Draw a bounding box around every leukocyte (white blood cell).
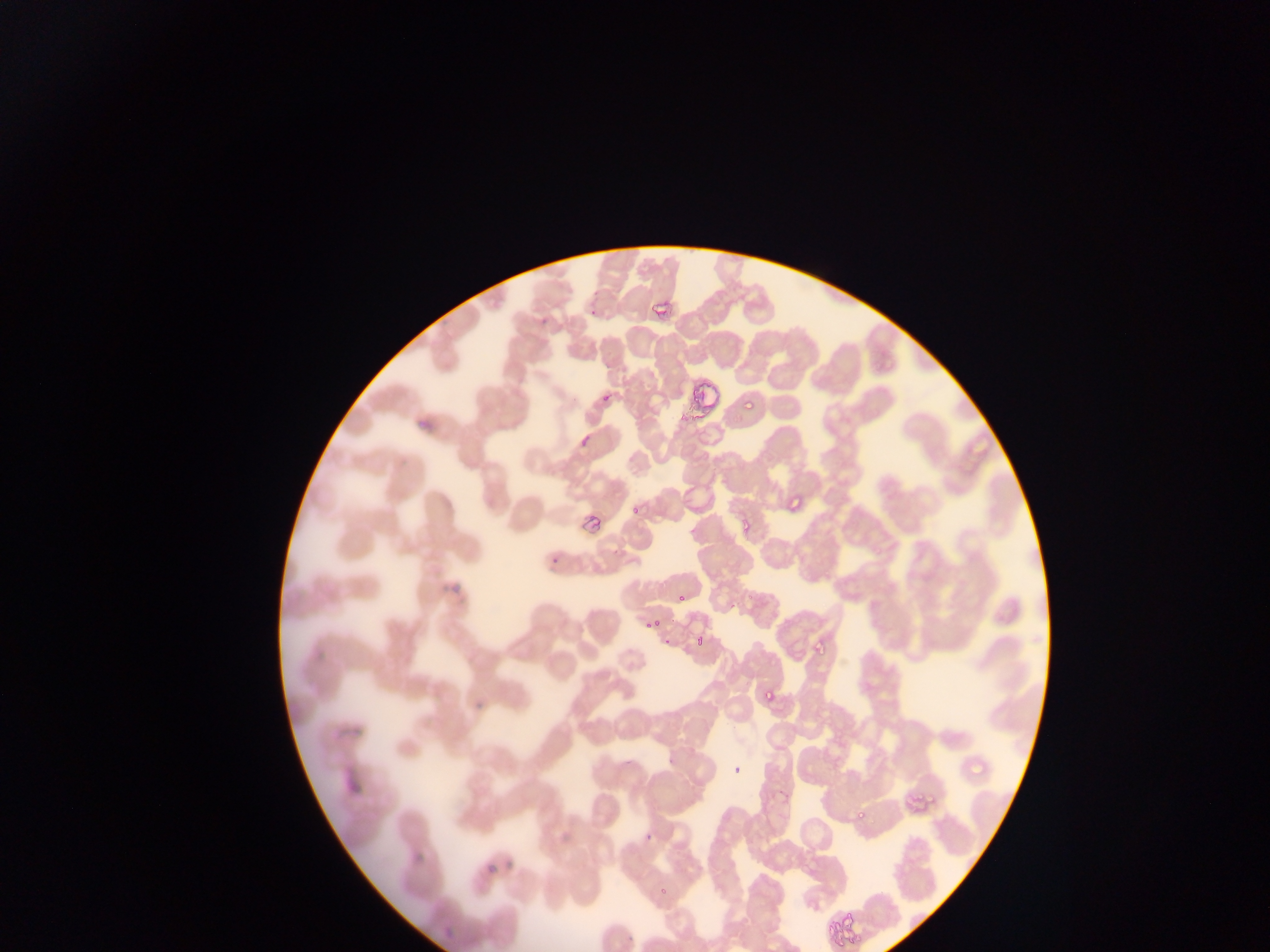
No leukocytes observed.

Approximate bounding boxes as [left, top, right, bottom] in pixels.
Summary:
  - Malaria parasite locations: [583, 286, 608, 314], [650, 294, 672, 325], [538, 304, 556, 329], [684, 351, 720, 417], [593, 390, 615, 405], [742, 398, 755, 411], [417, 411, 436, 432], [578, 425, 590, 452], [581, 482, 611, 534], [785, 493, 804, 513], [630, 505, 639, 515], [736, 521, 753, 533], [549, 547, 561, 564], [450, 580, 467, 597], [676, 592, 688, 603], [651, 617, 659, 625], [695, 634, 707, 647], [812, 635, 830, 656], [662, 636, 676, 653], [314, 645, 323, 671], [761, 686, 776, 702], [474, 698, 488, 711], [340, 722, 362, 747], [732, 760, 743, 777], [355, 771, 362, 787], [853, 806, 870, 821], [644, 829, 650, 840], [483, 855, 501, 876], [414, 857, 424, 866], [656, 883, 670, 898], [822, 906, 853, 945], [623, 917, 641, 950], [440, 927, 463, 943]
  - Capture: mobile-phone photograph through a microscope
  - Country: Ghana
  - Image size: 1270×952 pixels
  - Preparation: thin blood smear
  - Field of view: single